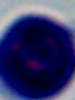

1000x magnification. Micrograph. A leukocyte is seen.